Name the parasite shown.
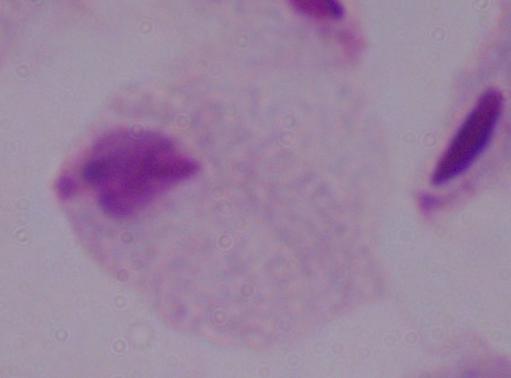
A trichomonad.

Summary:
  - Modality: photomicrograph
  - Magnification: 1000x